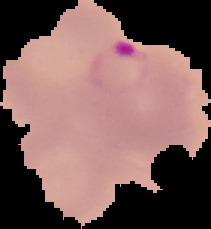
Summary:
  - Image size: 211×229 pixels
  - Malaria status: parasitized
  - Image type: segmented cell region on a black background
  - Preparation: thin blood film